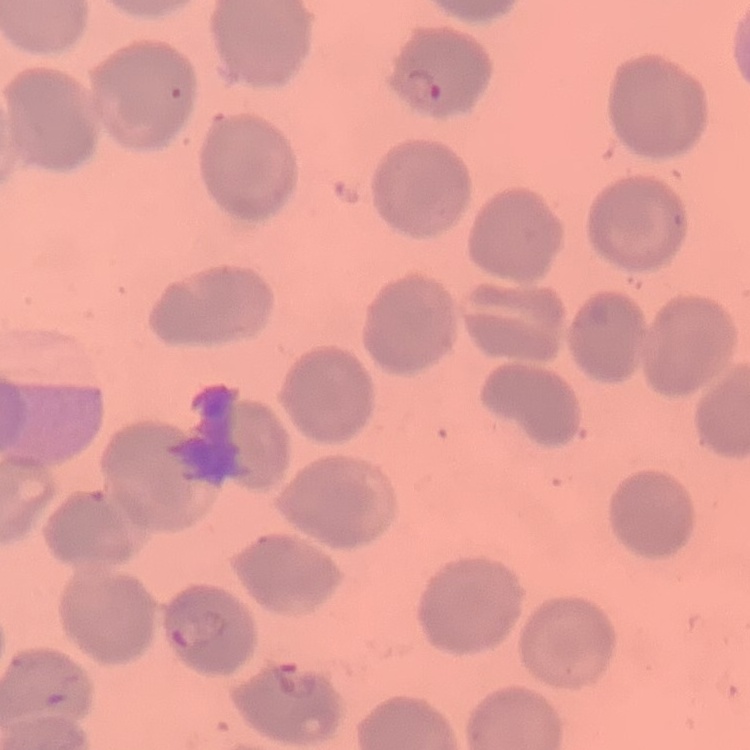

The red blood cells show no rouleaux formation. Square crop of a larger photomicrograph. Field's or Giemsa stain. Thin blood smear.